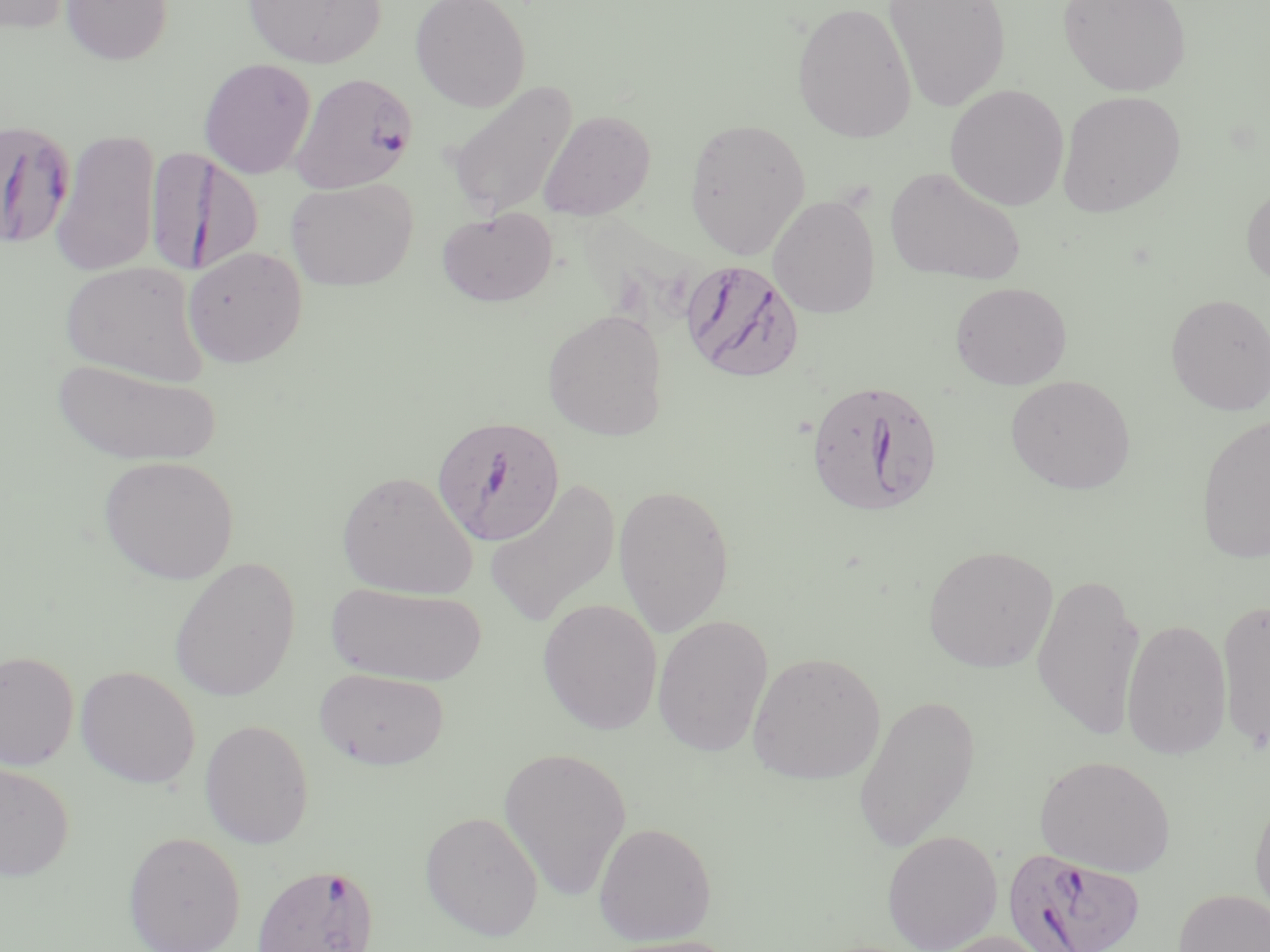
slide-level diagnosis = Plasmodium falciparum
preparation = thin blood smear
image size = 1270×952 pixels
field of view = one of a larger specimen
stain = May-Grünwald-Giemsa
Plasmodium falciparum-infected red blood cell locations = approximate bounding boxes as named x1/y1/x2/y2 corners in pixels: (x1=290, y1=72, x2=418, y2=193), (x1=0, y1=118, x2=75, y2=250), (x1=146, y1=147, x2=262, y2=275), (x1=684, y1=261, x2=802, y2=384), (x1=805, y1=377, x2=945, y2=518), (x1=431, y1=415, x2=566, y2=547), (x1=1001, y1=847, x2=1149, y2=952), (x1=251, y1=862, x2=381, y2=952)
magnification = 1000x
modality = light microscopy
uninfected red blood cell locations = approximate bounding boxes as named x1/y1/x2/y2 corners in pixels: (x1=0, y1=0, x2=75, y2=35), (x1=61, y1=0, x2=173, y2=65), (x1=243, y1=0, x2=385, y2=69), (x1=410, y1=0, x2=531, y2=112), (x1=883, y1=0, x2=1012, y2=112), (x1=1058, y1=0, x2=1192, y2=96), (x1=792, y1=1, x2=916, y2=144), (x1=198, y1=58, x2=316, y2=179), (x1=445, y1=80, x2=578, y2=220), (x1=944, y1=83, x2=1069, y2=210), (x1=1057, y1=90, x2=1187, y2=217), (x1=538, y1=110, x2=656, y2=221), (x1=684, y1=117, x2=811, y2=259), (x1=50, y1=128, x2=161, y2=277), (x1=885, y1=165, x2=1027, y2=285), (x1=286, y1=177, x2=418, y2=290), (x1=1241, y1=180, x2=1270, y2=292), (x1=768, y1=195, x2=881, y2=318), (x1=437, y1=208, x2=557, y2=307), (x1=182, y1=246, x2=308, y2=368), (x1=60, y1=260, x2=209, y2=387), (x1=950, y1=281, x2=1072, y2=389), (x1=1166, y1=293, x2=1270, y2=416), (x1=541, y1=308, x2=668, y2=441), (x1=51, y1=358, x2=223, y2=466), (x1=1005, y1=375, x2=1136, y2=494), (x1=1196, y1=412, x2=1270, y2=565), (x1=98, y1=455, x2=239, y2=584), (x1=336, y1=470, x2=478, y2=600), (x1=484, y1=479, x2=622, y2=628), (x1=613, y1=483, x2=735, y2=638), (x1=922, y1=544, x2=1058, y2=673), (x1=168, y1=557, x2=300, y2=703), (x1=1032, y1=570, x2=1145, y2=741), (x1=327, y1=581, x2=487, y2=687), (x1=1217, y1=597, x2=1270, y2=750), (x1=537, y1=599, x2=663, y2=734), (x1=652, y1=614, x2=774, y2=757), (x1=1121, y1=617, x2=1232, y2=760), (x1=0, y1=650, x2=80, y2=771), (x1=747, y1=650, x2=886, y2=785), (x1=76, y1=665, x2=200, y2=789), (x1=315, y1=667, x2=450, y2=771), (x1=853, y1=693, x2=981, y2=852), (x1=199, y1=719, x2=314, y2=849), (x1=498, y1=746, x2=632, y2=901), (x1=1035, y1=755, x2=1176, y2=876), (x1=0, y1=760, x2=75, y2=882), (x1=1249, y1=791, x2=1270, y2=926), (x1=419, y1=810, x2=544, y2=940), (x1=592, y1=821, x2=717, y2=945), (x1=881, y1=830, x2=1002, y2=951), (x1=123, y1=831, x2=246, y2=952), (x1=1174, y1=888, x2=1269, y2=952), (x1=930, y1=929, x2=1062, y2=952), (x1=597, y1=935, x2=744, y2=952)